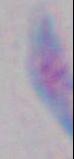
Summary:
  - Identification: Toxoplasma gondii
  - Modality: micrograph
  - Magnification: 1000x